Classify this cell by malaria status.
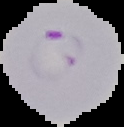
It is parasitized.

preparation = thin blood smear
image size = 124×127 pixels
image type = segmented cell region with the area outside set to black